Identify the parasite.
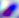
This is Toxoplasma gondii.

Summary:
  - Magnification: 400x
  - Modality: micrograph